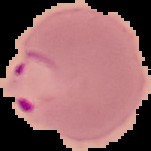
image type = segmented cell region on a black background
image size = 151×151 pixels
malaria status = parasitized
preparation = thin blood smear